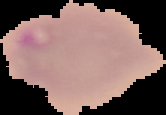

From a thin blood film. Malaria status: parasitized. The area outside the segmented cell region is set to black. Image is 166×115 pixels.